Name the cell type shown.
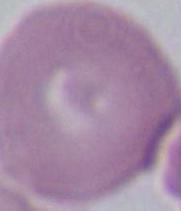
An erythrocyte.

magnification = 1000x
modality = micrograph